Classify this cell by malaria status.
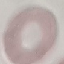
It is uninfected.

Summary:
  - Stain: Giemsa
  - Capture: smartphone camera at the microscope eyepiece
  - Preparation: thin blood film
  - Image type: cell patch, automatically extracted from a larger field of view and resized to 64 × 64 pixels